Assess this cell for malaria.
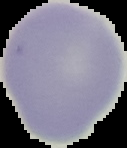
Uninfected.

Summary:
  - Image size: 127×148 pixels
  - Preparation: thin blood smear
  - Image type: segmented cell region with the area outside set to black